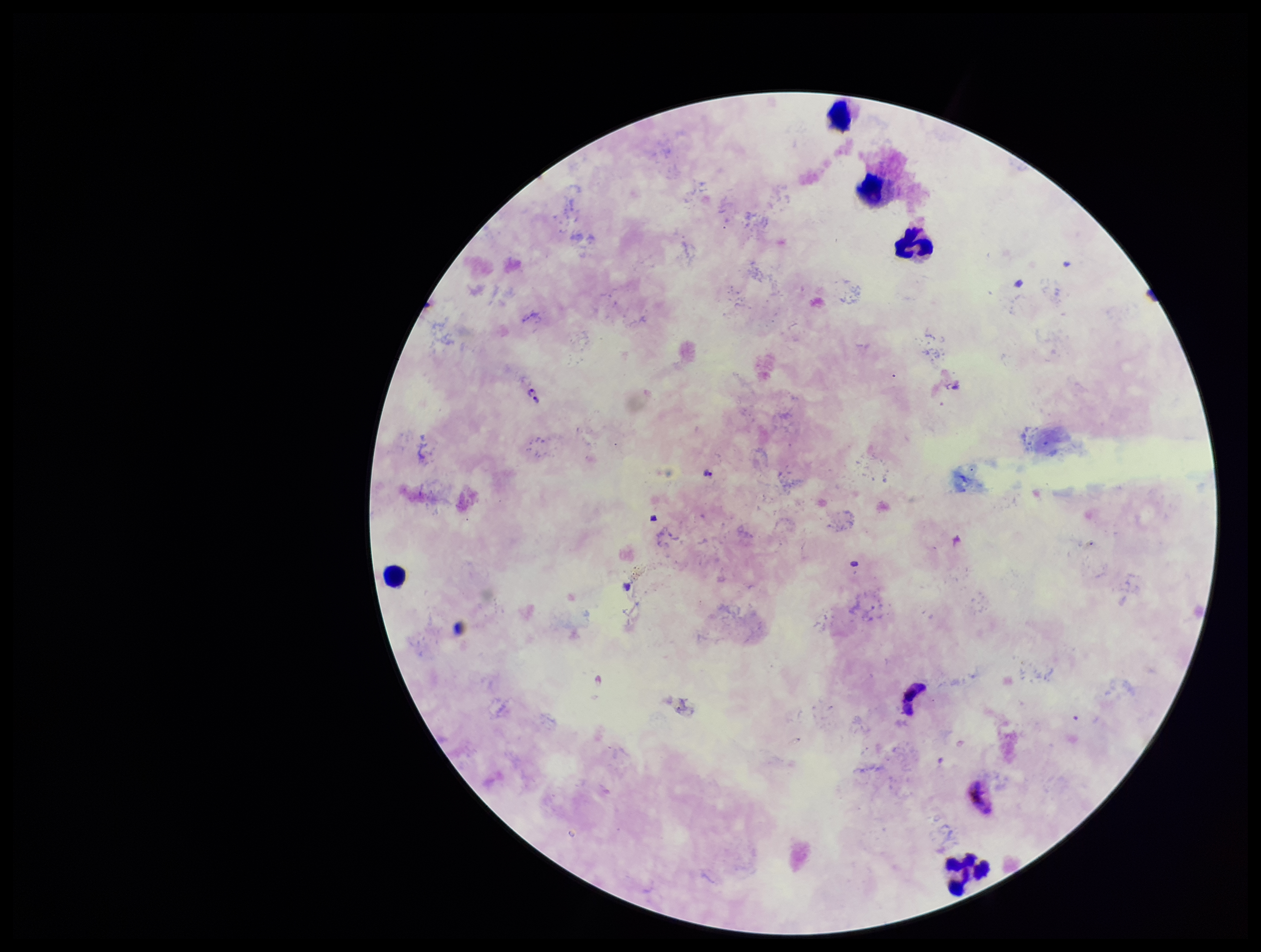
Summary:
  - Stain: Giemsa
  - Image size: 1261×952 pixels
  - Plasmodium parasites: identified
  - Species reported for this patient: Plasmodium falciparum
  - Leukocyte count: 5
  - Parasite count: 6
  - Field of view: one from this slide
  - Capture: smartphone photograph through the microscope eyepiece
  - Patient malaria status: positive
  - Preparation: thick